State the preparation type.
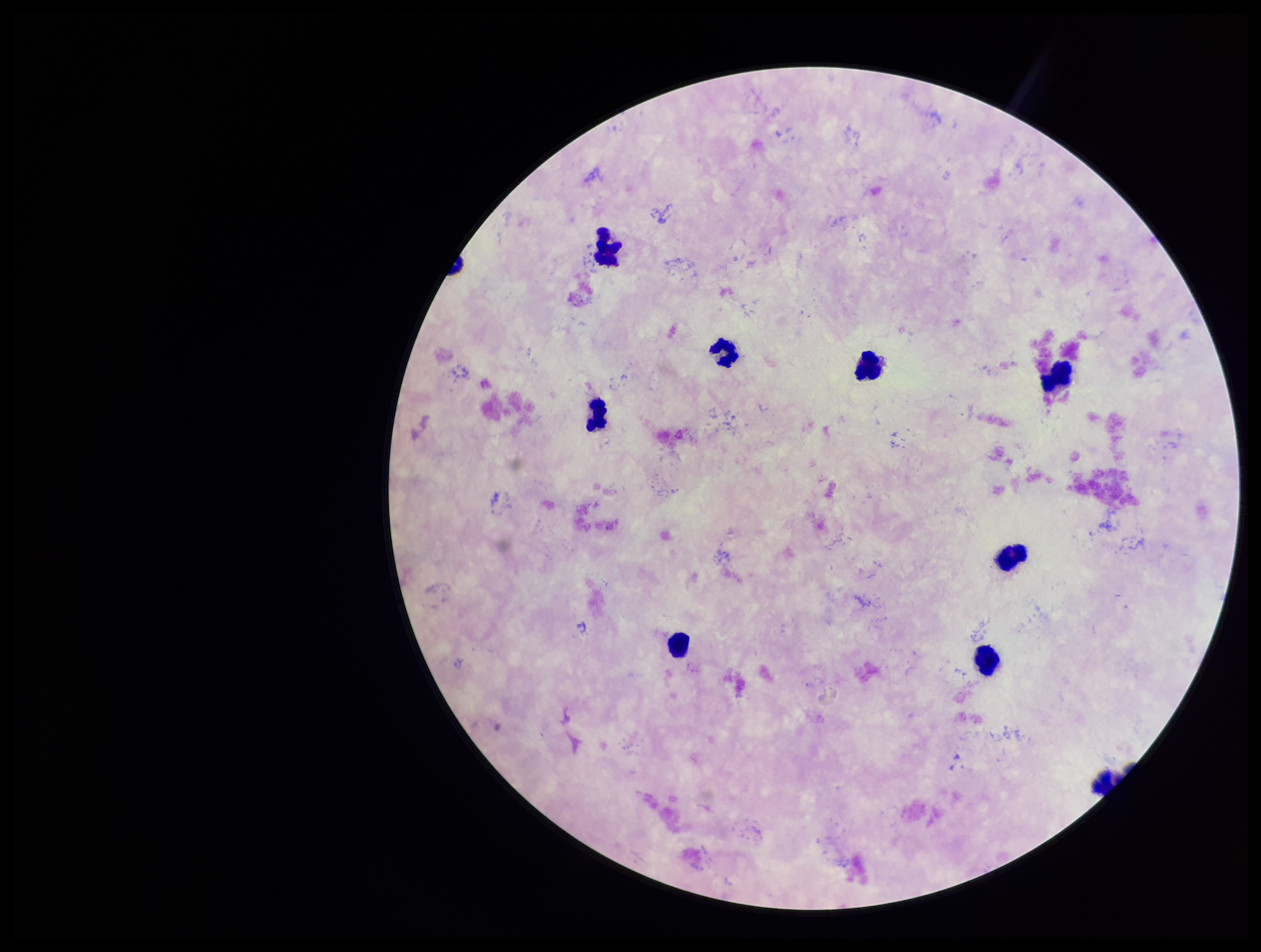

A thick smear.

Leukocyte count: 9. Smartphone photograph taken through the eyepiece of a microscope. One field from this slide. Patient malaria status: negative. Stained with Giemsa. Parasite count: 0. Image is 1261×952 pixels. Plasmodium parasites: none identified.